Classify this cell by malaria status.
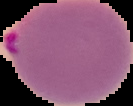

Parasitized.

From a thin blood film. Segmented cell region on a black background. Image is 133×106 pixels.